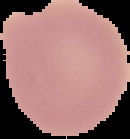 Malaria status: uninfected. Image is 130×139 pixels. From a thin blood smear. Segmented cell region on a black background.